Locate every blood parasite and identify its species.
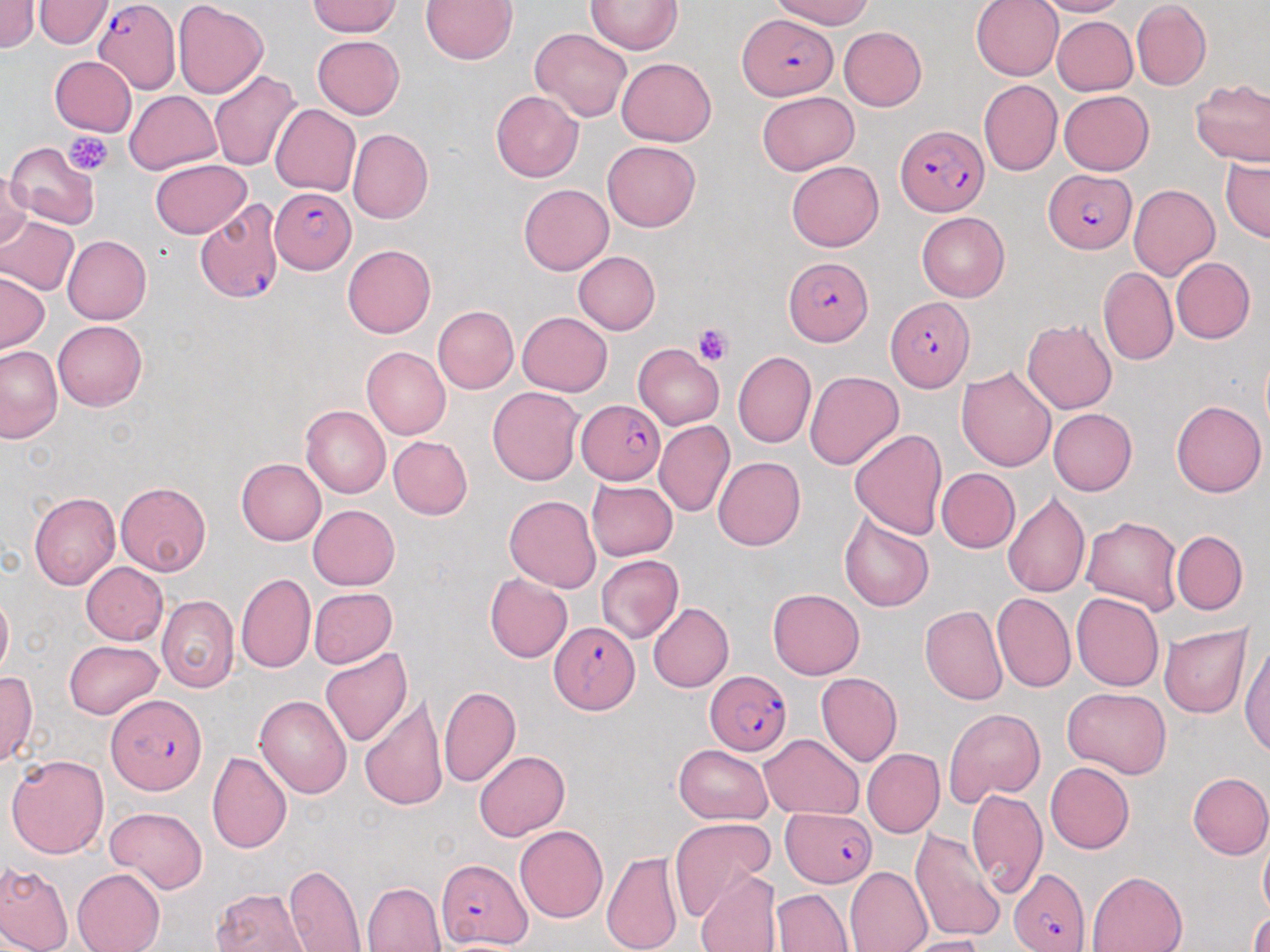

Approximate bounding boxes as [x1, y1, x2, y2] in pixels.
Plasmodium falciparum-infected red blood cells: [92, 1, 181, 94], [740, 14, 837, 100], [896, 125, 986, 218], [1043, 170, 1137, 253], [270, 189, 355, 272], [195, 197, 284, 305], [783, 254, 872, 346], [885, 297, 973, 391], [576, 398, 665, 483], [550, 621, 639, 712], [705, 669, 791, 755], [107, 695, 207, 794], [783, 809, 876, 888], [437, 858, 531, 949], [1009, 867, 1091, 951].
No Plasmodium ovale, Plasmodium malariae, Plasmodium vivax, Babesia divergens, or Trypanosoma brucei observed.

Platelet locations: [66, 132, 114, 175], [693, 324, 733, 366]. Uninfected red blood cell locations: [0, 0, 39, 53], [34, 0, 114, 49], [172, 0, 268, 99], [420, 0, 517, 65], [771, 0, 872, 30], [972, 0, 1064, 80], [1034, 0, 1129, 17], [307, 1, 400, 37], [585, 1, 682, 55], [1132, 2, 1210, 89], [1052, 16, 1138, 96], [838, 26, 926, 110], [529, 27, 632, 123], [312, 35, 405, 119], [50, 56, 137, 136], [616, 57, 716, 146], [210, 69, 303, 171], [1191, 78, 1270, 167], [979, 79, 1062, 176], [124, 90, 221, 174], [491, 90, 583, 183], [1059, 90, 1154, 175], [757, 91, 858, 175], [269, 104, 360, 196], [347, 128, 433, 224], [602, 140, 700, 232], [5, 141, 99, 230], [1221, 156, 1269, 242], [150, 159, 250, 238], [786, 161, 884, 252], [1, 172, 33, 251], [519, 184, 613, 274], [1129, 184, 1221, 281], [916, 212, 1010, 302], [0, 217, 80, 295], [62, 235, 151, 324], [342, 243, 436, 338], [573, 251, 660, 335], [1170, 257, 1255, 344], [1098, 266, 1178, 366], [0, 271, 49, 353], [433, 305, 519, 393], [517, 311, 613, 395], [1022, 318, 1117, 415], [53, 319, 147, 410], [979, 329, 1108, 444], [633, 344, 724, 429], [0, 346, 62, 443], [363, 347, 451, 440], [733, 352, 816, 448], [956, 366, 1057, 471], [804, 370, 904, 470], [487, 386, 585, 485], [1171, 399, 1266, 497], [300, 406, 390, 498], [1048, 408, 1137, 496], [654, 421, 734, 517], [849, 428, 947, 538], [388, 436, 473, 518], [713, 457, 805, 551], [236, 458, 326, 546], [936, 468, 1020, 554], [586, 479, 677, 560], [116, 481, 211, 576], [1002, 491, 1089, 597], [29, 493, 120, 590], [504, 494, 601, 593], [307, 504, 399, 590], [838, 512, 933, 612], [1080, 516, 1184, 615], [1172, 530, 1248, 615], [596, 555, 684, 643], [81, 562, 168, 644], [483, 572, 571, 663], [236, 573, 315, 674], [309, 587, 397, 669], [767, 588, 864, 679], [0, 589, 12, 680], [1071, 591, 1164, 692], [993, 592, 1076, 692], [156, 595, 239, 692], [647, 603, 733, 692], [920, 605, 1007, 705], [1160, 624, 1251, 718], [1239, 640, 1269, 759], [64, 641, 163, 719], [321, 647, 413, 748], [0, 672, 37, 766], [816, 672, 902, 766], [438, 685, 521, 787], [1062, 686, 1172, 780], [254, 694, 352, 799], [359, 696, 447, 811], [945, 708, 1044, 804], [760, 734, 864, 820], [673, 744, 774, 824], [862, 749, 945, 837], [474, 750, 569, 841], [207, 751, 292, 854], [7, 754, 109, 858], [1045, 761, 1134, 854], [1187, 772, 1270, 859], [966, 788, 1047, 899], [104, 807, 208, 894], [670, 817, 778, 921], [514, 824, 608, 924], [909, 828, 1005, 945], [1259, 833, 1270, 918], [601, 850, 683, 952], [0, 859, 73, 952], [283, 863, 367, 951], [844, 866, 931, 952], [72, 867, 165, 952], [1087, 870, 1187, 952], [694, 871, 782, 952], [361, 882, 447, 951], [210, 887, 312, 951], [773, 889, 853, 951], [1249, 911, 1270, 952], [895, 934, 987, 952]. Slide-level diagnosis: Plasmodium falciparum. Thin blood smear. Captured at 1000x magnification. Optical microscopy. Image is 1270×952 pixels. Single field of view. May-Grünwald-Giemsa-stained preparation.